Report the malaria status of this cell.
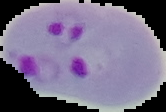
It is parasitized.

Summary:
  - Image type: segmented cell region with the area outside set to black
  - Image size: 166×112 pixels
  - Preparation: thin blood film